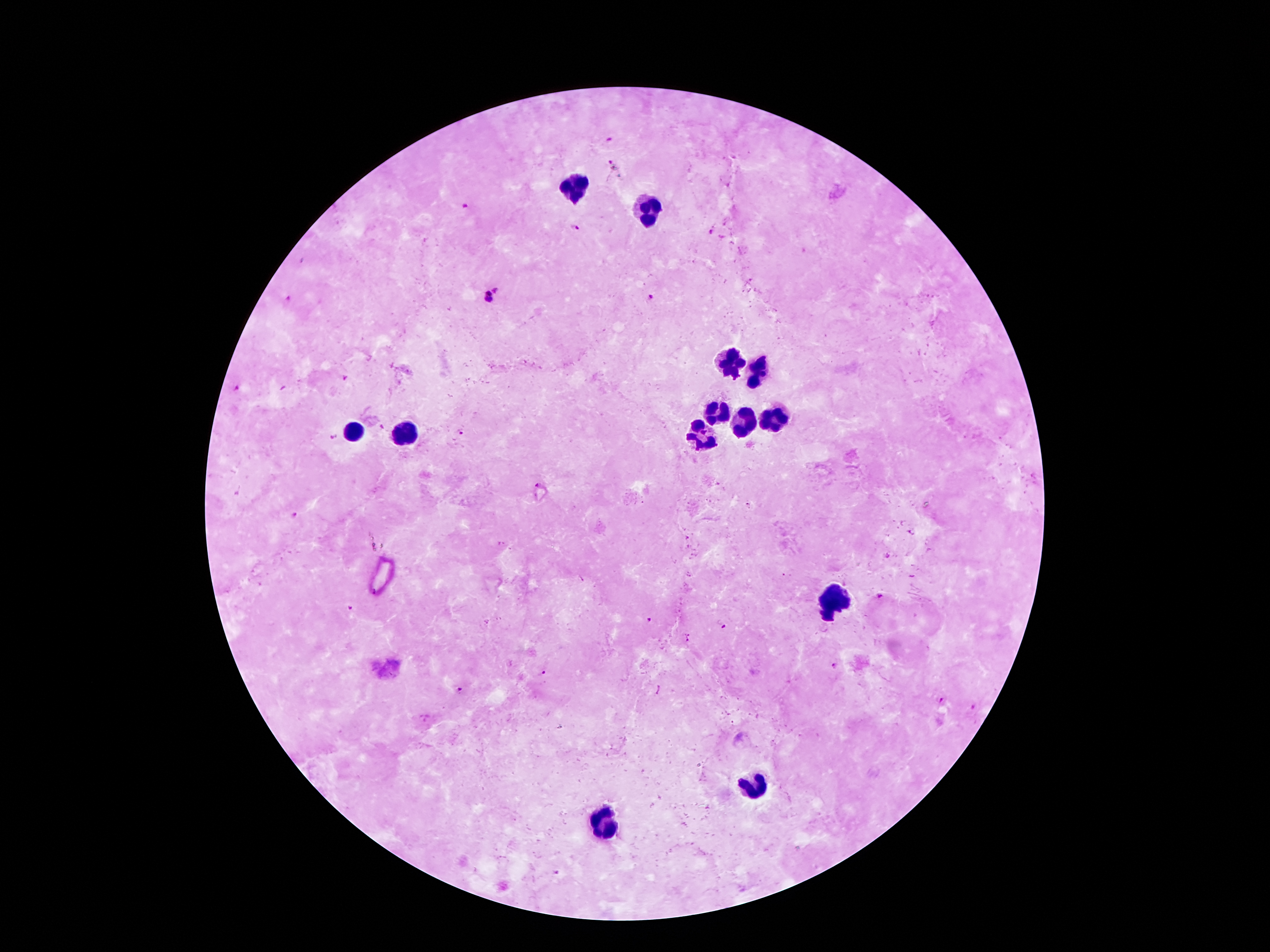

{
  "magnification": "100x",
  "patient_malaria_status": "positive for Plasmodium falciparum",
  "malaria_parasite_locations": "approximate centers as (x, y) in pixels: (609, 138), (611, 164), (463, 208), (576, 228), (710, 232), (497, 288), (650, 296), (288, 298), (484, 300), (345, 377), (236, 388), (463, 431), (334, 438), (537, 484), (748, 505), (296, 516), (879, 599), (349, 608), (650, 618), (724, 628), (689, 638), (836, 666), (544, 672), (461, 689), (943, 700), (975, 708)",
  "stain": "Giemsa",
  "leukocyte_locations": "approximate centers as (x, y) in pixels: (577, 188), (650, 209), (729, 363), (758, 373), (717, 414), (776, 417), (745, 423), (402, 427), (354, 432), (706, 435), (829, 597), (752, 789), (606, 826)",
  "capture": "smartphone camera through the microscope eyepiece",
  "field_of_view": "single",
  "image_size": "1270×952 pixels",
  "preparation": "thick peripheral-blood smear"
}